Locate every uninfected red blood cell.
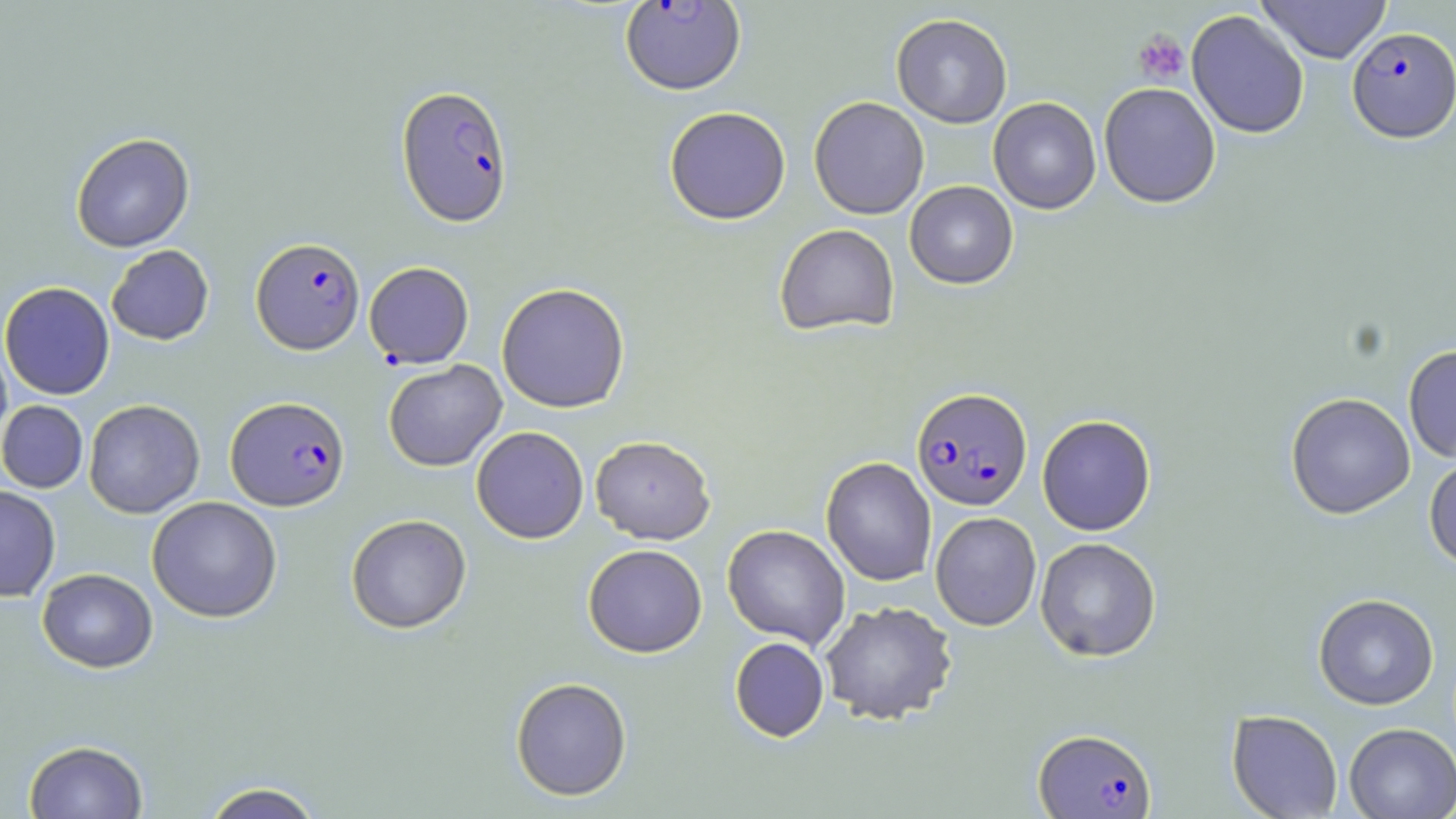

Approximate bounding boxes as named x1/y1/x2/y2 corners in pixels.
Uninfected red blood cells: (x1=1257, y1=0, x2=1392, y2=64), (x1=1186, y1=10, x2=1310, y2=139), (x1=891, y1=13, x2=1012, y2=128), (x1=1098, y1=82, x2=1222, y2=208), (x1=808, y1=96, x2=929, y2=219), (x1=988, y1=97, x2=1101, y2=214), (x1=664, y1=106, x2=791, y2=225), (x1=70, y1=133, x2=195, y2=253), (x1=904, y1=181, x2=1018, y2=289), (x1=774, y1=223, x2=900, y2=336), (x1=106, y1=245, x2=214, y2=345), (x1=0, y1=281, x2=115, y2=400), (x1=496, y1=282, x2=630, y2=413), (x1=0, y1=335, x2=13, y2=451), (x1=1403, y1=344, x2=1456, y2=463), (x1=383, y1=359, x2=506, y2=472), (x1=1285, y1=392, x2=1415, y2=519), (x1=83, y1=399, x2=205, y2=518), (x1=0, y1=400, x2=88, y2=493), (x1=1037, y1=414, x2=1156, y2=536), (x1=471, y1=426, x2=589, y2=543), (x1=590, y1=435, x2=715, y2=544), (x1=1424, y1=452, x2=1456, y2=571), (x1=821, y1=456, x2=937, y2=586), (x1=0, y1=485, x2=60, y2=602), (x1=147, y1=496, x2=283, y2=622), (x1=930, y1=511, x2=1042, y2=631), (x1=346, y1=514, x2=472, y2=634), (x1=722, y1=524, x2=851, y2=649), (x1=1035, y1=536, x2=1161, y2=662), (x1=583, y1=543, x2=708, y2=658), (x1=37, y1=568, x2=158, y2=673), (x1=1313, y1=593, x2=1439, y2=710), (x1=819, y1=600, x2=958, y2=725), (x1=729, y1=636, x2=829, y2=742), (x1=510, y1=677, x2=632, y2=801), (x1=1227, y1=709, x2=1343, y2=819), (x1=1344, y1=723, x2=1456, y2=818), (x1=23, y1=740, x2=148, y2=818), (x1=199, y1=781, x2=327, y2=819).

Summary:
  - Platelet locations: (x1=1133, y1=30, x2=1190, y2=85)
  - Plasmodium falciparum-infected red blood cell locations: (x1=620, y1=0, x2=746, y2=95), (x1=1347, y1=26, x2=1455, y2=142), (x1=396, y1=85, x2=513, y2=227), (x1=251, y1=237, x2=365, y2=354), (x1=364, y1=262, x2=473, y2=368), (x1=911, y1=387, x2=1033, y2=511), (x1=225, y1=395, x2=350, y2=511), (x1=1034, y1=727, x2=1157, y2=818)
  - Slide-level diagnosis: Plasmodium falciparum
  - Field of view: one of a larger specimen
  - Stain: May-Grünwald-Giemsa
  - Image size: 1456×819 pixels
  - Magnification: 1000x
  - Preparation: thin blood smear
  - Modality: light microscopy